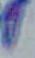
modality = photomicrograph
magnification = 1000x
identification = Toxoplasma gondii